Name the blood parasite species.
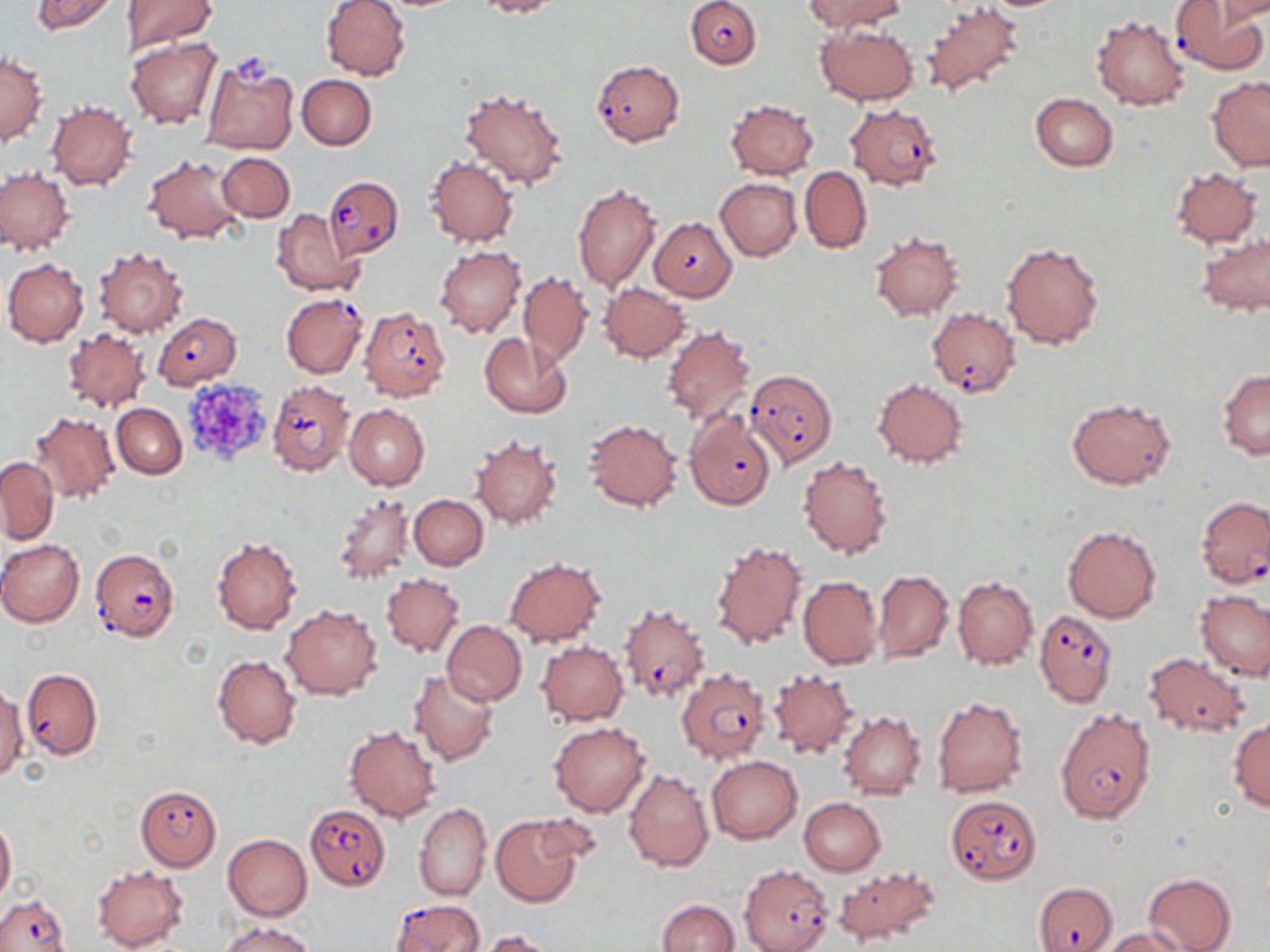
Plasmodium falciparum.

magnification = 1000x
platelet locations = approximate bounding boxes as (x1, y1, x2, y2) in pixels: (231, 46, 276, 84), (182, 375, 275, 464)
image size = 1270×952 pixels
modality = light microscopy
Plasmodium falciparum-infected red blood cell locations = approximate bounding boxes as (x1, y1, x2, y2) in pixels: (685, 0, 761, 68), (1170, 2, 1267, 73), (591, 59, 685, 147), (844, 103, 941, 190), (323, 176, 401, 260), (649, 215, 738, 301), (281, 293, 368, 377), (359, 306, 451, 401), (927, 307, 1021, 397), (152, 312, 242, 388), (745, 369, 838, 466), (266, 379, 353, 474), (685, 412, 775, 510), (1197, 497, 1270, 588), (89, 549, 179, 643), (619, 602, 711, 703), (1034, 610, 1117, 707), (22, 668, 102, 759), (676, 668, 770, 765), (1054, 709, 1155, 823), (135, 784, 221, 871), (945, 794, 1043, 884), (303, 803, 391, 890), (739, 864, 834, 952), (1034, 880, 1118, 952), (0, 893, 71, 952), (390, 899, 485, 951)
stain = May-Grünwald-Giemsa
preparation = thin blood film
uninfected red blood cell locations = approximate bounding boxes as (x1, y1, x2, y2) in pixels: (30, 0, 121, 36), (121, 0, 216, 54), (319, 0, 411, 80), (475, 0, 560, 18), (802, 0, 906, 33), (1215, 1, 1270, 25), (923, 4, 1026, 97), (1090, 14, 1190, 110), (815, 23, 919, 105), (125, 36, 224, 130), (1, 54, 47, 146), (199, 57, 299, 157), (297, 75, 377, 149), (1206, 76, 1270, 170), (459, 85, 570, 190), (1029, 92, 1118, 171), (46, 100, 136, 191), (725, 100, 819, 179), (217, 152, 294, 222), (143, 153, 247, 244), (424, 155, 518, 249), (800, 166, 873, 253), (1170, 167, 1262, 248), (0, 168, 74, 254), (715, 178, 801, 261), (571, 182, 661, 294), (272, 208, 363, 296), (870, 231, 963, 320), (1196, 232, 1270, 317), (1001, 238, 1107, 351), (435, 244, 527, 338), (94, 246, 188, 337), (2, 257, 89, 347), (518, 271, 592, 367), (599, 283, 691, 361), (660, 324, 756, 425), (62, 328, 150, 412), (480, 333, 573, 418), (1217, 369, 1270, 459), (871, 377, 968, 469), (1066, 397, 1175, 488), (111, 403, 186, 478), (344, 404, 429, 491), (29, 411, 120, 503), (582, 419, 682, 511), (471, 434, 563, 530), (798, 455, 893, 559), (0, 456, 58, 543), (332, 492, 416, 586), (409, 494, 488, 569), (1062, 524, 1161, 622), (211, 535, 302, 634), (709, 537, 807, 650), (0, 539, 85, 627), (504, 557, 607, 646), (874, 569, 953, 663), (381, 572, 465, 658), (953, 575, 1038, 671), (798, 576, 883, 669), (1196, 591, 1270, 680), (282, 604, 383, 700), (441, 620, 526, 706), (537, 641, 628, 724), (1142, 651, 1253, 738), (212, 654, 302, 749), (408, 668, 500, 768), (766, 669, 860, 760), (1, 686, 27, 782), (931, 696, 1028, 798), (838, 711, 927, 801), (1228, 719, 1270, 810), (548, 721, 651, 817), (343, 723, 441, 822), (707, 754, 802, 844), (624, 768, 715, 872), (799, 798, 887, 876), (412, 801, 492, 901), (528, 813, 606, 867), (491, 815, 583, 906), (0, 817, 16, 901), (222, 833, 311, 920), (834, 863, 940, 946), (91, 865, 188, 951), (1143, 873, 1236, 952), (656, 899, 739, 952), (220, 921, 315, 952), (1100, 928, 1188, 951), (476, 929, 561, 951)
field of view = one of a larger specimen